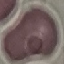
Result: no malaria parasites detected. Giemsa-stained preparation. Acquired by smartphone through the microscope eyepiece. Cell patch, automatically extracted from a larger field of view and resized to 64 × 64 pixels. Thin blood film.